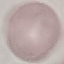

Summary:
  - Result: negative for malaria parasites
  - Preparation: thin smear
  - Capture: smartphone camera at the microscope eyepiece
  - Stain: Giemsa
  - Image type: cell patch, automatically extracted from a larger field of view and resized to 64 × 64 pixels